Name the blood parasite species.
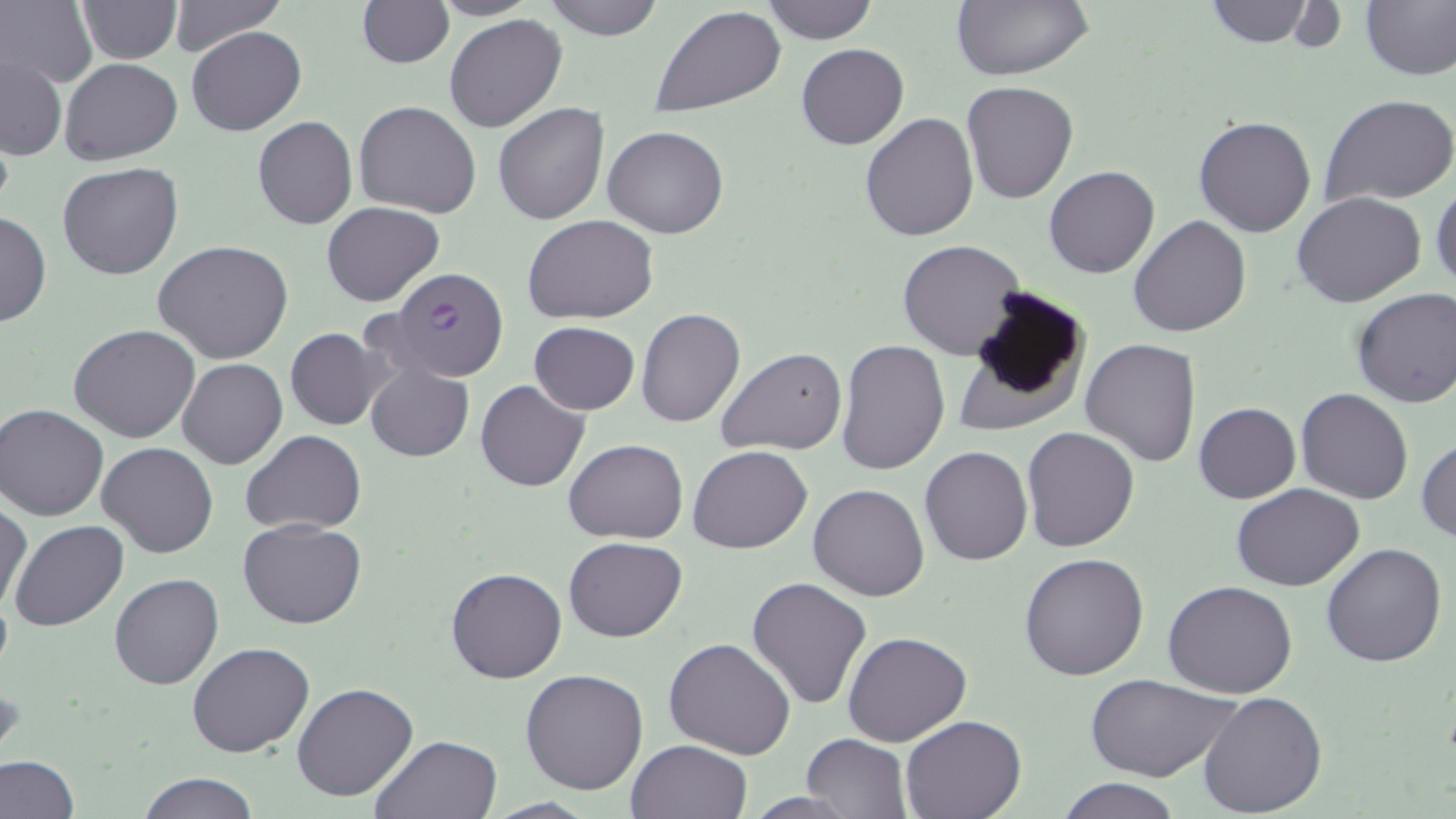
Plasmodium falciparum.

Summary:
  - Coordinate format: approximate bounding boxes as (x1, y1, x2, y2) in pixels
  - Uninfected red blood cell locations: (75, 0, 181, 63), (166, 0, 287, 56), (356, 0, 453, 67), (430, 0, 537, 20), (544, 0, 664, 40), (762, 0, 876, 44), (950, 0, 1095, 81), (1202, 0, 1313, 47), (1360, 0, 1456, 80), (1, 1, 96, 89), (652, 6, 786, 116), (444, 14, 567, 133), (187, 25, 306, 135), (795, 43, 909, 150), (2, 56, 67, 158), (60, 57, 181, 165), (962, 80, 1078, 204), (1323, 95, 1456, 204), (353, 100, 482, 218), (493, 103, 609, 225), (859, 114, 980, 242), (1194, 115, 1318, 238), (252, 116, 357, 230), (603, 125, 729, 238), (58, 162, 184, 280), (1043, 165, 1160, 279), (1431, 180, 1455, 294), (1293, 191, 1426, 309), (323, 202, 445, 306), (0, 211, 50, 327), (524, 215, 660, 324), (1128, 216, 1252, 337), (153, 239, 294, 363), (898, 240, 1025, 359), (962, 285, 1091, 415), (1351, 287, 1456, 408), (635, 307, 745, 428), (529, 322, 639, 414), (68, 325, 201, 442), (286, 327, 388, 430), (1080, 338, 1201, 467), (835, 339, 950, 476), (717, 348, 846, 458), (178, 357, 287, 468), (365, 361, 473, 461), (476, 380, 589, 491), (1296, 388, 1413, 505), (1193, 401, 1301, 504), (1, 402, 109, 521), (1020, 426, 1140, 552), (240, 430, 366, 532), (1416, 437, 1456, 545), (564, 438, 688, 544), (96, 442, 218, 558), (688, 445, 812, 554), (920, 446, 1033, 565), (808, 483, 930, 601), (1231, 484, 1364, 592), (1, 501, 31, 617), (238, 518, 365, 629), (8, 521, 128, 632), (565, 536, 687, 640), (1320, 542, 1447, 667), (1020, 553, 1150, 679), (445, 565, 567, 683), (109, 573, 224, 690), (746, 576, 871, 710), (1162, 581, 1298, 699), (842, 631, 972, 746), (664, 637, 795, 759), (187, 641, 314, 757), (520, 668, 650, 795), (1082, 674, 1240, 784), (293, 683, 419, 802), (1198, 689, 1328, 815), (900, 715, 1026, 819), (802, 732, 911, 817), (370, 733, 504, 819), (625, 739, 752, 819), (0, 754, 78, 818), (140, 772, 258, 819), (1055, 777, 1183, 819)
  - Plasmodium falciparum-infected red blood cell locations: (387, 269, 508, 379)
  - Modality: light microscopy
  - Field of view: one of a larger specimen
  - Preparation: thin blood smear
  - Stain: May-Grünwald-Giemsa
  - Image size: 1456×819 pixels
  - Magnification: 1000x